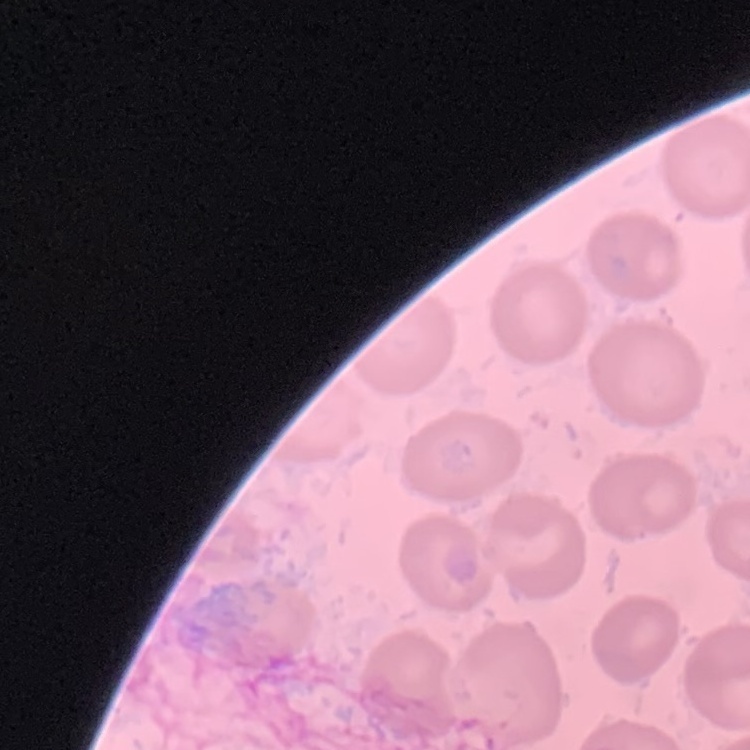
erythrocyte morphology = no rouleaux formation
image type = one tile cut from a larger photomicrograph
preparation = thin blood smear
stain = Field's or Giemsa